Give the extent of all Plasmodium parasites.
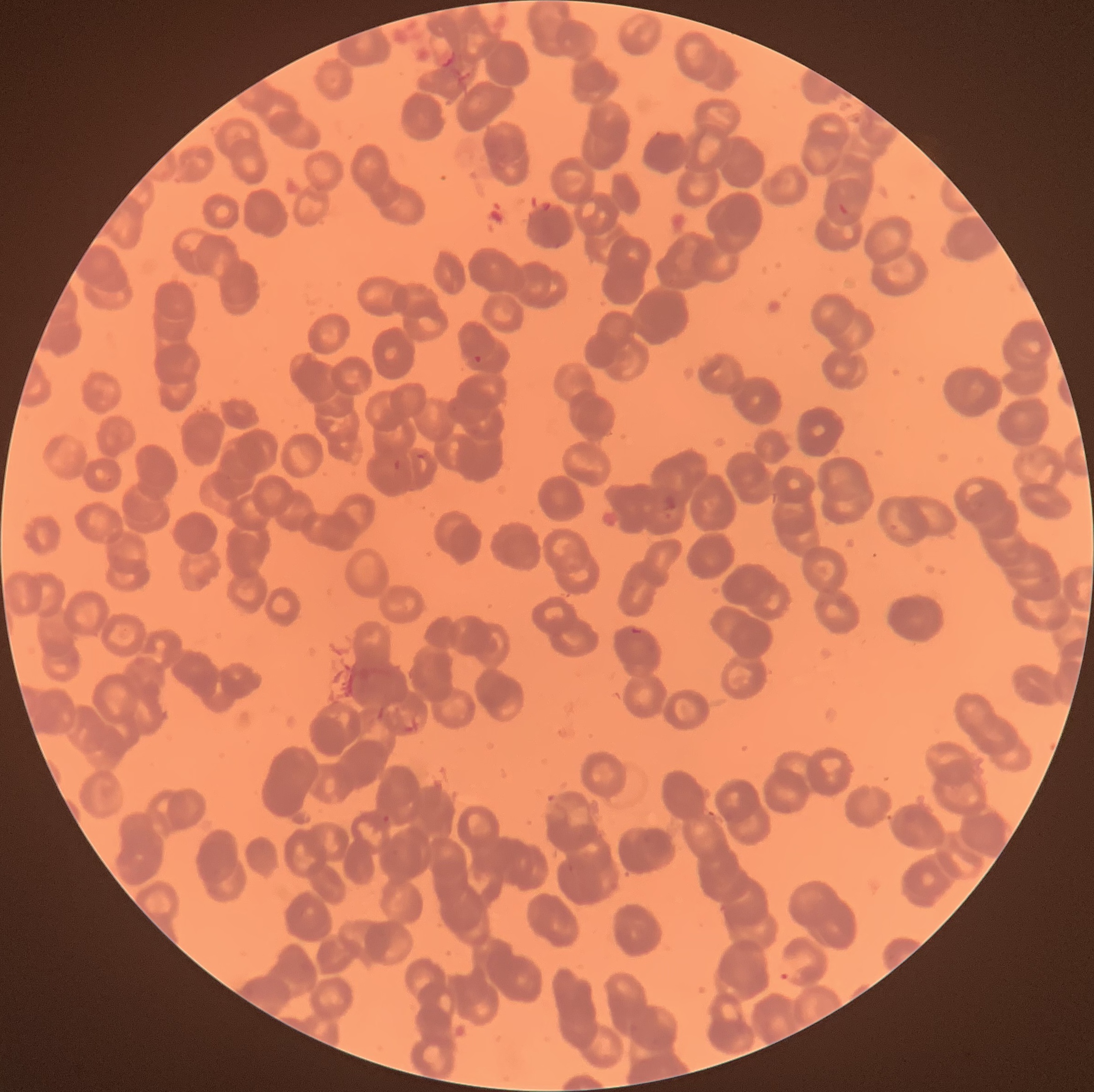
Approximate bounding boxes as [x1, y1, x2, y2] in pixels.
Plasmodium parasites: [467, 354, 483, 364], [414, 452, 432, 462], [392, 459, 402, 470], [380, 814, 392, 825], [779, 955, 809, 983].

Optical microscopy. Image is 1094×1092 pixels. The red blood cells show rouleaux formation. Thin blood film.